Identify the parasite.
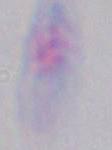

Toxoplasma gondii.

Photomicrograph. 1000x magnification.